Identify the preparation type.
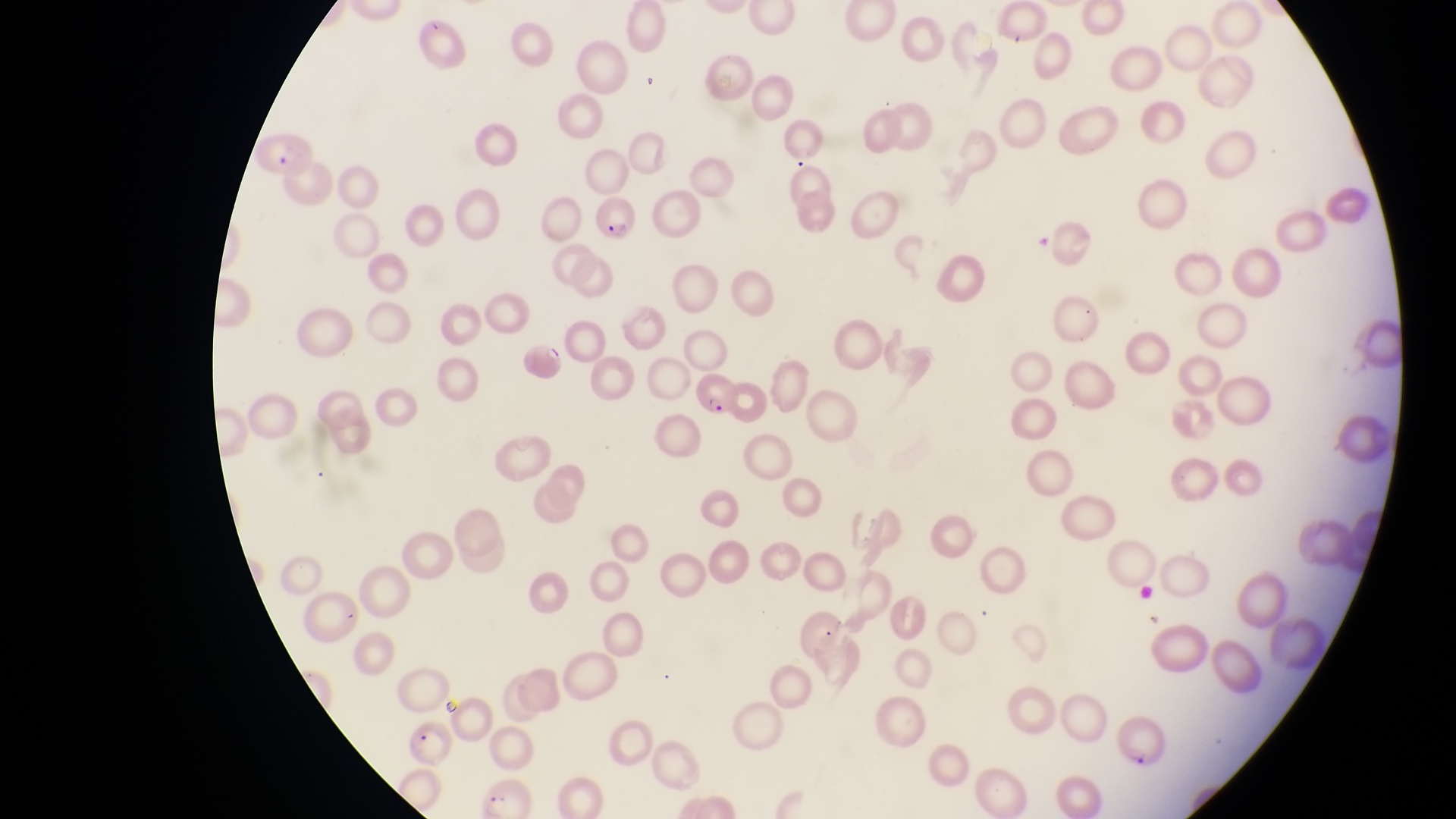

Thin blood smear.

capture = smartphone photograph through the eyepiece of an Olympus CX-23 microscope
parasitised red blood cell locations = approximate bounding boxes as left top right bottom in pixels: 257 129 316 182; 592 199 641 248; 516 338 565 385; 693 373 742 419; 1118 717 1171 772
country = Uganda
field of view = single
magnification = 1000x
image size = 1456×819 pixels